Give the position of every leukocyte visible.
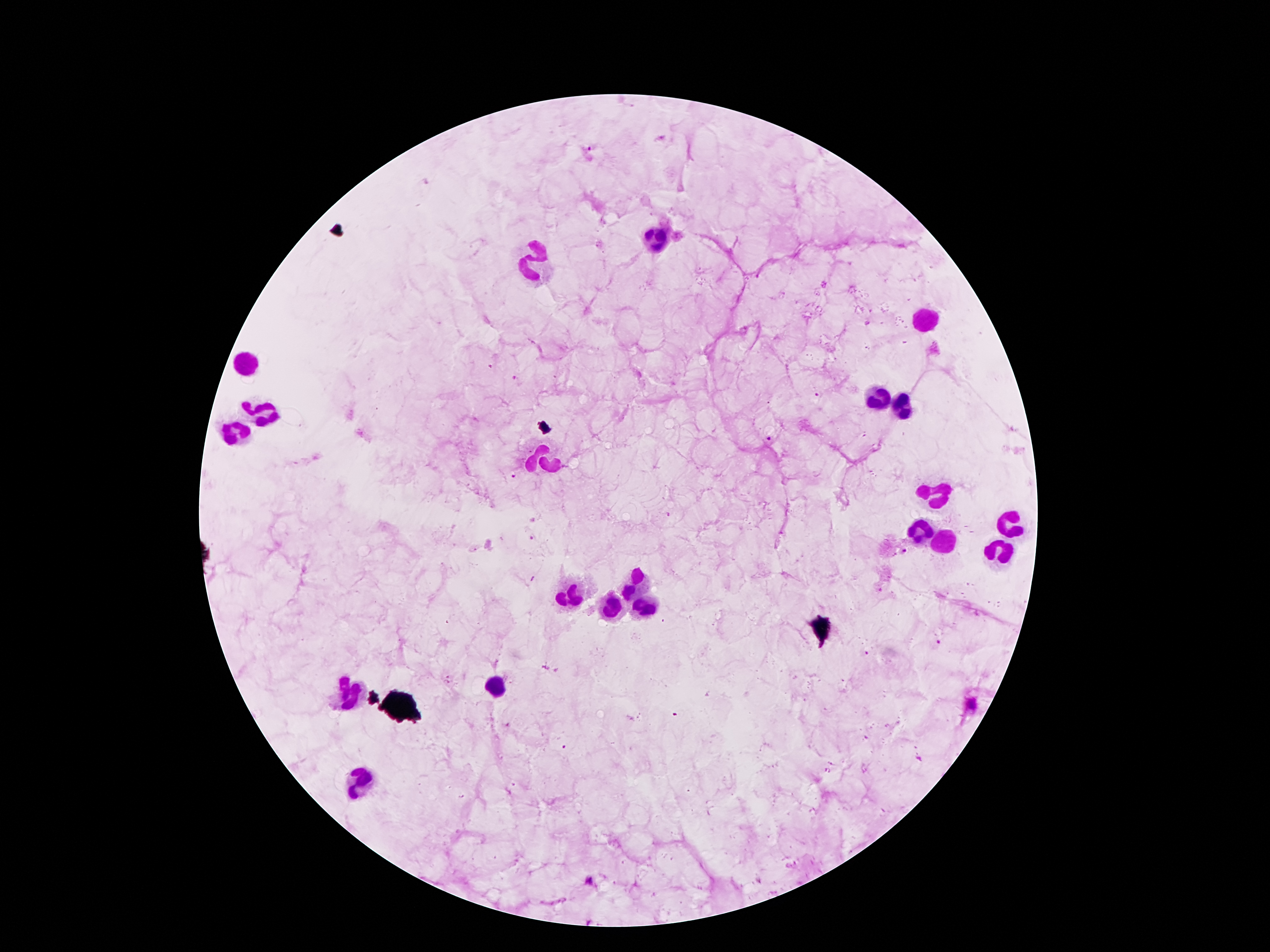

Approximate centers as {x, y} in pixels.
Leukocytes: {658, 239}, {536, 263}, {925, 321}, {251, 362}, {878, 397}, {906, 407}, {266, 410}, {234, 433}, {544, 461}, {936, 489}, {1010, 524}, {923, 532}, {945, 541}, {1003, 550}, {632, 584}, {570, 595}, {641, 606}, {607, 608}, {493, 685}, {350, 692}, {359, 782}.

{
  "field_of_view": "one from this slide",
  "patient_malaria_status": "positive for Plasmodium falciparum",
  "preparation": "thick blood smear",
  "image_size": "1270×952 pixels",
  "capture": "smartphone camera through the microscope eyepiece",
  "stain": "Giemsa",
  "plasmodium_parasite_locations": "approximate centers as {x, y} in pixels: {490, 366}, {515, 378}, {817, 395}, {766, 438}, {512, 477}, {530, 539}, {906, 552}, {938, 641}, {867, 653}, {547, 669}, {448, 678}, {587, 881}",
  "magnification": "100x"
}